Describe the morphology of the erythrocytes.
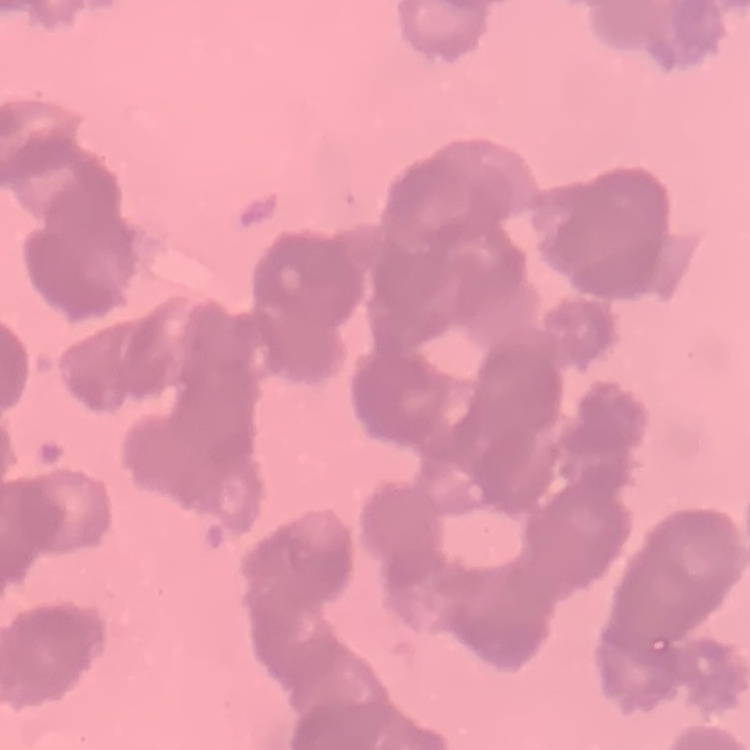
They show rouleaux formation.

stain = Field's or Giemsa
image type = square crop of a larger photomicrograph
preparation = thin blood film